Identify the parasite.
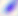

Toxoplasma gondii.

Summary:
  - Modality: micrograph
  - Magnification: 400x